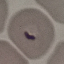

{
  "malaria_status": "parasitized",
  "image_type": "automatically extracted cell patch, resized to 64 × 64 pixels",
  "preparation": "thin blood smear",
  "capture": "smartphone through the microscope eyepiece",
  "stain": "Giemsa"
}